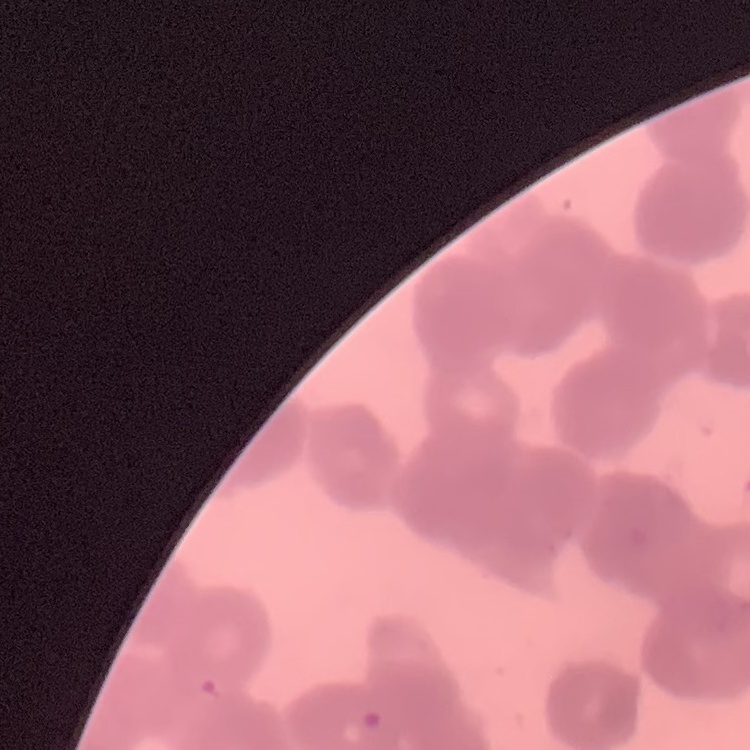

red blood cell morphology = rouleaux formation
stain = Field's or Giemsa
preparation = thin blood film
image type = one tile cut from a larger photomicrograph